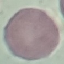

{
  "malaria_status": "uninfected",
  "image_type": "cell patch, automatically extracted from a larger field of view and resized to 64 × 64 pixels",
  "preparation": "thin blood film",
  "capture": "smartphone camera at the microscope eyepiece",
  "stain": "Giemsa"
}